Mark where platelets are.
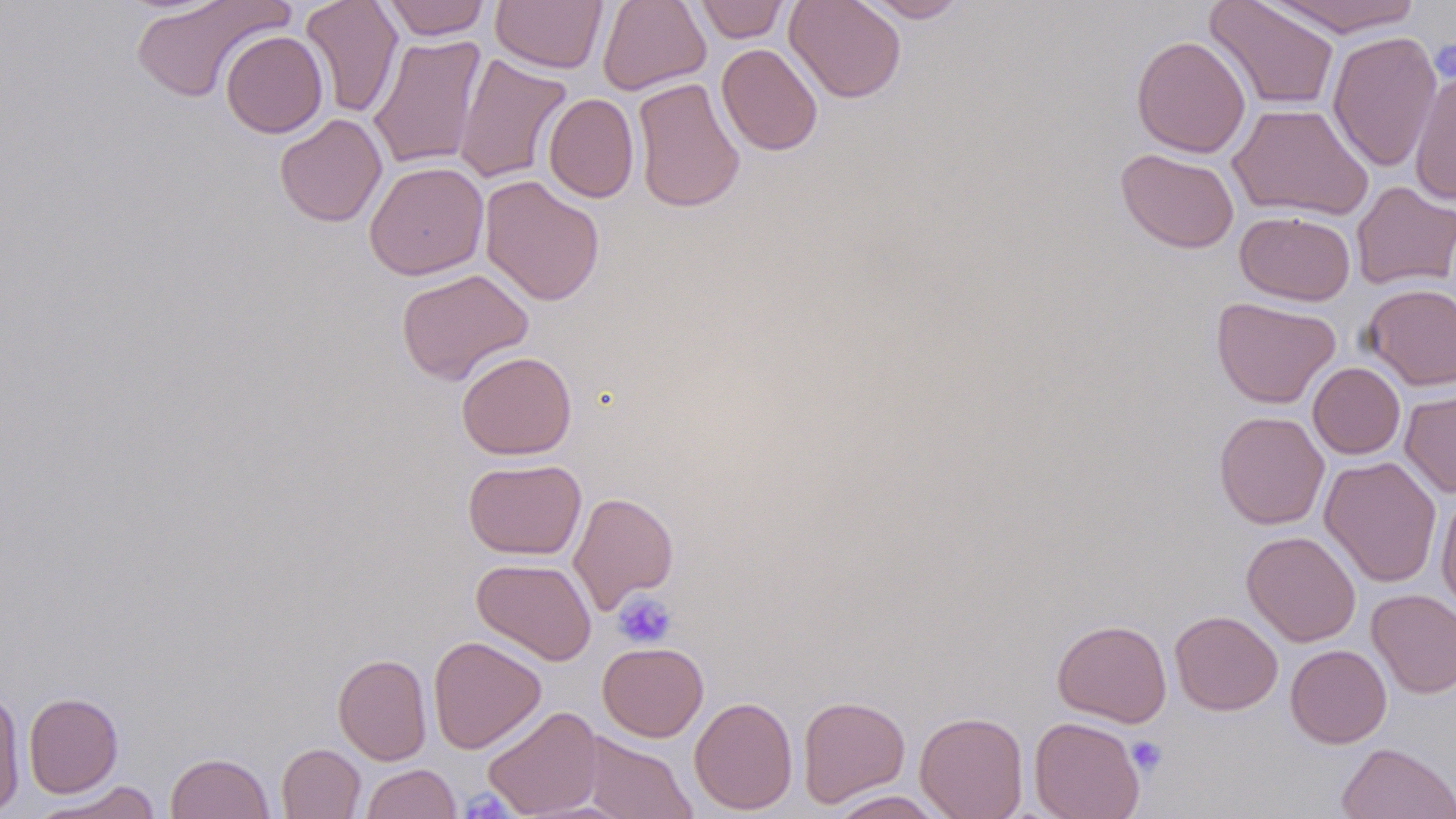

Approximate bounding boxes as (x1, y1, x2, y2) in pixels.
Platelets: (612, 591, 677, 649), (1126, 736, 1167, 776), (461, 788, 512, 819).

Summary:
  - Uninfected red blood cell locations: (130, 0, 289, 103), (300, 0, 403, 118), (379, 0, 491, 40), (491, 0, 608, 73), (597, 0, 711, 95), (692, 0, 792, 43), (784, 0, 907, 103), (860, 0, 970, 22), (1265, 0, 1423, 36), (1205, 1, 1340, 112), (220, 30, 328, 138), (1327, 31, 1442, 173), (368, 34, 487, 170), (1131, 35, 1251, 158), (716, 43, 823, 156), (453, 53, 572, 185), (1409, 69, 1456, 205), (632, 77, 745, 213), (543, 93, 639, 203), (1227, 102, 1374, 221), (274, 113, 387, 227), (1115, 148, 1240, 253), (364, 161, 489, 280), (479, 175, 605, 306), (1351, 181, 1456, 290), (1235, 210, 1356, 305), (395, 268, 534, 385), (1362, 283, 1456, 391), (1211, 296, 1340, 408), (456, 351, 577, 460), (1308, 362, 1405, 459), (1400, 389, 1456, 499), (1213, 411, 1329, 530), (1319, 456, 1442, 587), (462, 459, 586, 559), (1435, 489, 1456, 615), (568, 491, 679, 613), (1241, 531, 1361, 647), (471, 558, 597, 666), (1366, 589, 1456, 698), (1170, 610, 1283, 715), (1051, 619, 1172, 727), (428, 635, 546, 754), (597, 642, 708, 741), (1285, 644, 1392, 748), (333, 653, 432, 765), (0, 691, 26, 815), (24, 692, 123, 798), (797, 694, 910, 807), (689, 696, 798, 815), (482, 705, 603, 818), (915, 711, 1029, 819), (1029, 716, 1145, 818), (581, 732, 697, 818), (1337, 742, 1456, 819), (276, 743, 366, 819), (165, 751, 275, 819), (361, 764, 461, 819), (32, 782, 163, 819), (826, 790, 950, 818)
  - Slide-level diagnosis: negative for blood parasites
  - Field of view: single
  - Modality: optical microscopy
  - Magnification: 1000x
  - Stain: May-Grünwald-Giemsa
  - Image size: 1456×819 pixels
  - Preparation: thin blood smear